Evaluate for malaria.
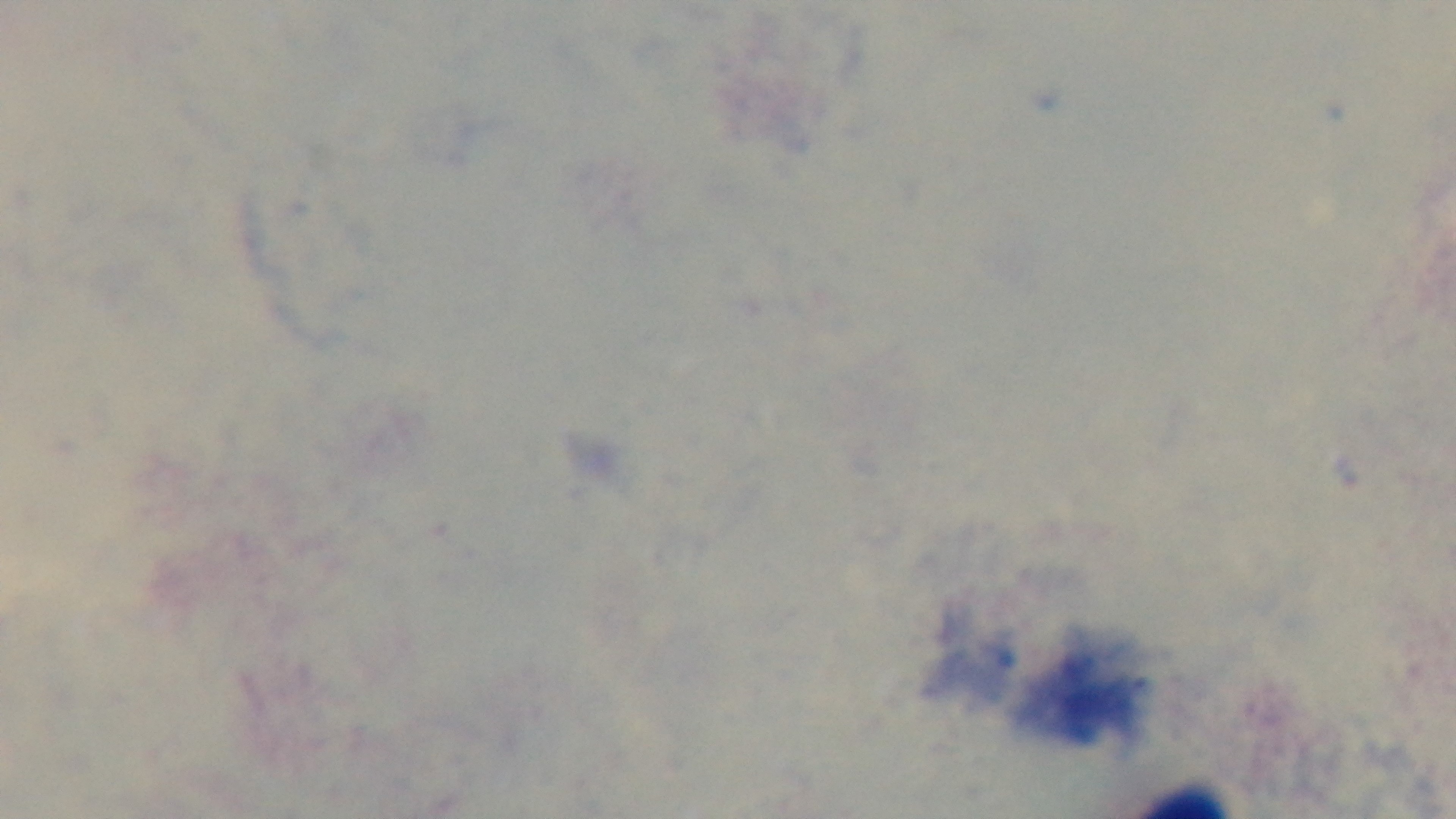

It is uninfected.

Single field of view. 100x oil-immersion objective. Preparation: thick. Light microscopy. Captured with a mounted 4K digital camera. Giemsa stain.